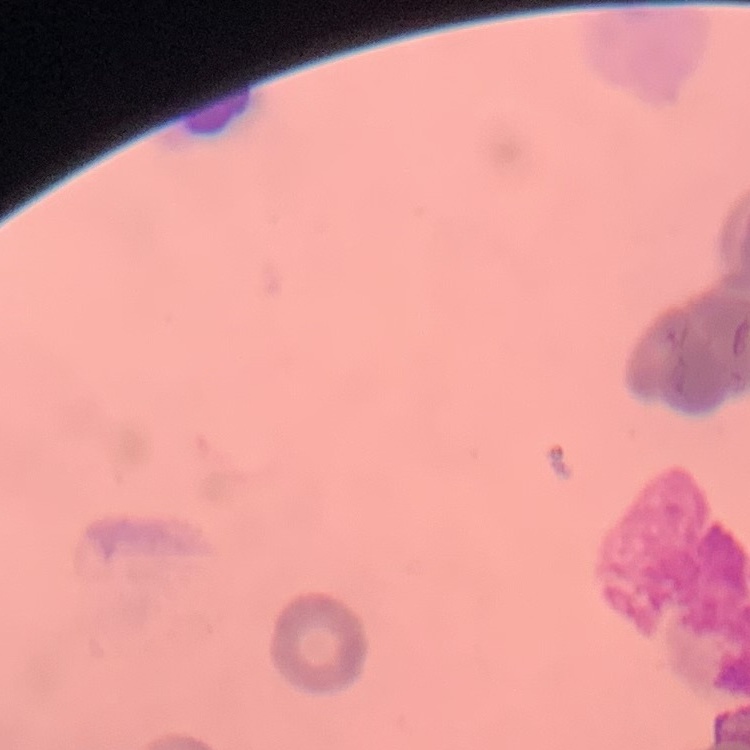

erythrocyte morphology = rouleaux formation
stain = Field's or Giemsa
image type = square crop of a larger photomicrograph
preparation = thin blood smear